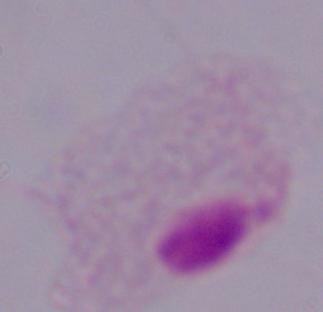
Micrograph. A trichomonad is shown. Captured at 1000x magnification.